Mark where platelets are.
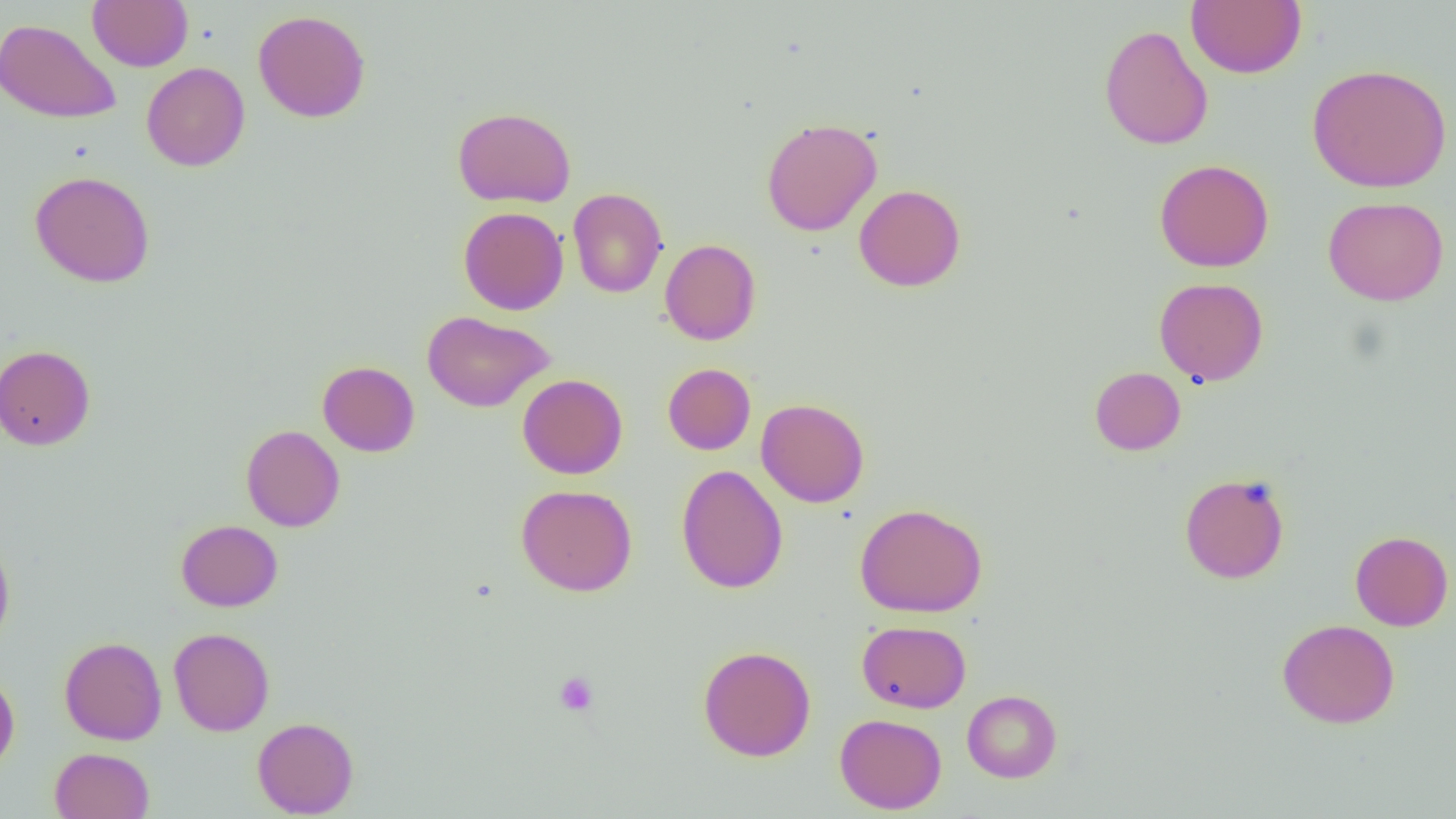
Approximate bounding boxes as named x1/y1/x2/y2 corners in pixels.
Platelets: (x1=554, y1=671, x2=599, y2=715).

{
  "slide_level_diagnosis": "no evidence of blood parasites",
  "modality": "light microscopy",
  "magnification": "1000x",
  "preparation": "thin blood smear",
  "image_size": "1456×819 pixels",
  "uninfected_red_blood_cell_locations": "approximate bounding boxes as named x1/y1/x2/y2 corners in pixels: (x1=88, y1=0, x2=193, y2=71), (x1=1186, y1=0, x2=1306, y2=78), (x1=252, y1=10, x2=371, y2=123), (x1=0, y1=17, x2=121, y2=123), (x1=1098, y1=24, x2=1213, y2=150), (x1=141, y1=62, x2=250, y2=171), (x1=1307, y1=63, x2=1452, y2=193), (x1=452, y1=106, x2=576, y2=208), (x1=761, y1=117, x2=882, y2=236), (x1=1154, y1=158, x2=1274, y2=272), (x1=29, y1=170, x2=155, y2=287), (x1=854, y1=184, x2=966, y2=292), (x1=568, y1=188, x2=668, y2=298), (x1=1323, y1=196, x2=1449, y2=306), (x1=458, y1=206, x2=569, y2=315), (x1=660, y1=239, x2=761, y2=345), (x1=1154, y1=277, x2=1269, y2=386), (x1=422, y1=310, x2=554, y2=412), (x1=0, y1=344, x2=95, y2=450), (x1=317, y1=360, x2=420, y2=457), (x1=662, y1=363, x2=756, y2=455), (x1=1089, y1=366, x2=1186, y2=455), (x1=517, y1=374, x2=627, y2=479), (x1=756, y1=398, x2=870, y2=507), (x1=241, y1=425, x2=345, y2=532), (x1=676, y1=465, x2=788, y2=594), (x1=1179, y1=472, x2=1290, y2=584), (x1=516, y1=484, x2=637, y2=596), (x1=855, y1=502, x2=988, y2=618), (x1=176, y1=520, x2=283, y2=611), (x1=1350, y1=530, x2=1453, y2=631), (x1=0, y1=534, x2=15, y2=649), (x1=1277, y1=618, x2=1400, y2=728), (x1=857, y1=620, x2=971, y2=713), (x1=168, y1=627, x2=274, y2=736), (x1=59, y1=636, x2=167, y2=745), (x1=698, y1=645, x2=816, y2=761), (x1=0, y1=671, x2=20, y2=776), (x1=962, y1=689, x2=1062, y2=782), (x1=835, y1=713, x2=946, y2=814), (x1=252, y1=716, x2=359, y2=817), (x1=50, y1=747, x2=154, y2=819)",
  "field_of_view": "single"
}